Assess this cell for malaria.
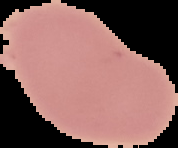
It is uninfected.

image size = 178×148 pixels
preparation = thin blood film
image type = segmented cell region on a black background